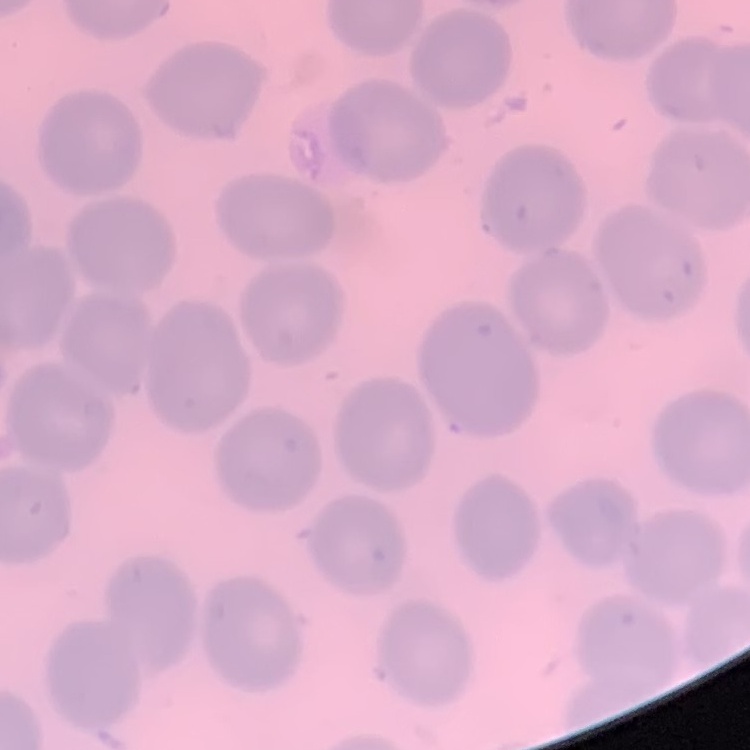

The erythrocytes show no rouleaux formation. Field's or Giemsa stain. Square crop of a larger photomicrograph. Thin blood smear.